Outline platelets.
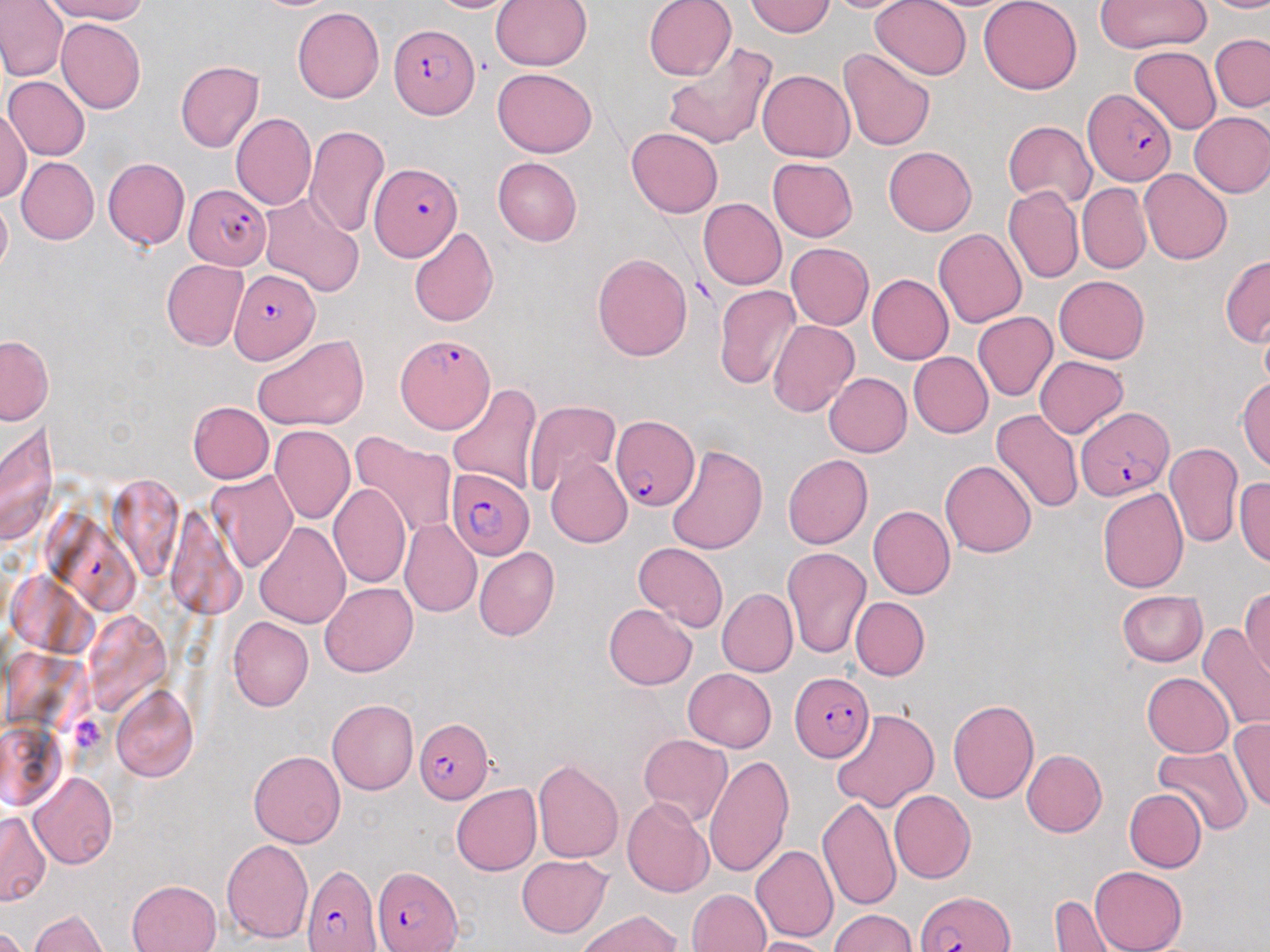

Approximate bounding boxes as [x1, y1, x2, y2] in pixels.
Platelets: [68, 714, 107, 756].

slide-level diagnosis = Plasmodium falciparum
magnification = 1000x
uninfected red blood cell locations (subset) = approximate bounding boxes as [x1, y1, x2, y2] in pixels: [0, 0, 68, 82], [46, 0, 148, 24], [425, 0, 523, 13], [643, 0, 738, 81], [819, 0, 921, 12], [869, 0, 973, 80], [979, 0, 1082, 95], [1092, 0, 1211, 52], [1203, 0, 1270, 14], [491, 1, 591, 71], [745, 1, 836, 37], [291, 7, 385, 103], [56, 19, 145, 115], [1210, 34, 1270, 112], [662, 44, 777, 149], [1130, 47, 1221, 135], [837, 48, 935, 152], [174, 61, 263, 153], [492, 68, 597, 159], [757, 69, 855, 163], [3, 76, 90, 161], [0, 106, 30, 203], [1190, 111, 1270, 198], [231, 113, 316, 212], [1003, 119, 1096, 210], [305, 125, 390, 237], [626, 127, 722, 218], [883, 146, 977, 236], [16, 157, 98, 245], [103, 157, 189, 249], [767, 157, 858, 241], [491, 158, 582, 246], [1140, 169, 1231, 264], [1077, 183, 1152, 273], [1004, 186, 1084, 283], [0, 193, 11, 280], [259, 193, 364, 297], [698, 198, 786, 289], [409, 226, 499, 328], [933, 228, 1027, 328], [786, 242, 873, 329], [592, 253, 693, 361], [1220, 254, 1270, 348], [161, 259, 249, 351], [867, 273, 953, 365], [1055, 275, 1149, 363], [714, 285, 800, 389], [974, 311, 1057, 401], [1259, 317, 1270, 395], [768, 320, 860, 418], [1, 335, 52, 424], [253, 335, 370, 433], [909, 352, 992, 437], [1035, 356, 1127, 437], [824, 373, 911, 457], [1237, 377, 1270, 472], [448, 382, 543, 490], [187, 401, 273, 483], [525, 401, 623, 496], [991, 409, 1083, 515], [0, 421, 59, 547], [269, 425, 354, 525], [350, 432, 456, 539], [1164, 443, 1242, 548], [667, 444, 767, 555], [547, 455, 633, 548], [783, 455, 873, 550], [941, 458, 1037, 557], [206, 471, 299, 572], [1235, 476, 1270, 567], [329, 483, 411, 589], [1097, 487, 1188, 593], [868, 505, 955, 600], [165, 506, 246, 617], [399, 519, 481, 617], [254, 522, 350, 630], [634, 542, 728, 631], [781, 545, 872, 658], [473, 547, 560, 640], [320, 582, 417, 678], [717, 588, 797, 676], [1241, 589, 1270, 681], [1117, 590, 1207, 667], [851, 597, 930, 681], [604, 603, 697, 690], [227, 616, 314, 712], [1198, 624, 1270, 731], [683, 668, 776, 752], [1143, 673, 1233, 756], [110, 684, 198, 782], [327, 698, 418, 795], [948, 698, 1039, 804], [829, 707, 940, 810], [1228, 718, 1270, 812], [0, 722, 67, 810], [639, 733, 732, 828], [1152, 746, 1253, 835], [1022, 749, 1107, 837], [249, 750, 346, 848], [704, 754, 794, 879], [532, 759, 623, 864], [29, 773, 117, 868], [451, 784, 541, 875], [1123, 788, 1206, 873], [889, 790, 975, 883], [623, 796, 715, 897], [817, 796, 901, 913], [0, 811, 50, 906], [221, 839, 314, 944], [752, 844, 838, 942], [517, 855, 613, 937], [1090, 867, 1187, 952], [126, 879, 222, 952], [688, 888, 771, 951], [1050, 893, 1116, 951], [828, 908, 917, 952], [27, 910, 110, 952], [575, 910, 684, 952], [0, 924, 33, 952], [747, 936, 836, 952]
image size = 1270×952 pixels
modality = light microscopy
preparation = thin blood film
field of view = single
Plasmodium falciparum-infected red blood cell locations (subset) = approximate bounding boxes as [x1, y1, x2, y2] in pixels: [389, 24, 478, 119], [1082, 88, 1177, 186], [185, 185, 271, 270], [230, 268, 320, 364], [395, 334, 495, 436], [1076, 407, 1173, 500], [611, 415, 701, 510], [445, 469, 535, 560], [789, 673, 875, 762], [415, 718, 494, 803], [302, 863, 382, 952], [915, 892, 1015, 951]
stain = May-Grünwald-Giemsa